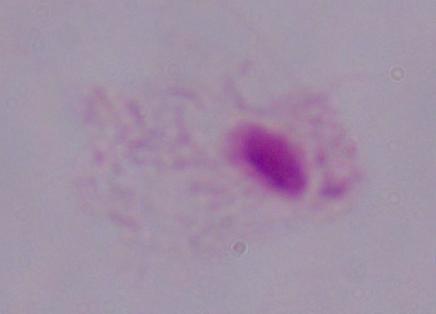

Summary:
  - Identification: trichomonad
  - Modality: photomicrograph
  - Magnification: 1000x